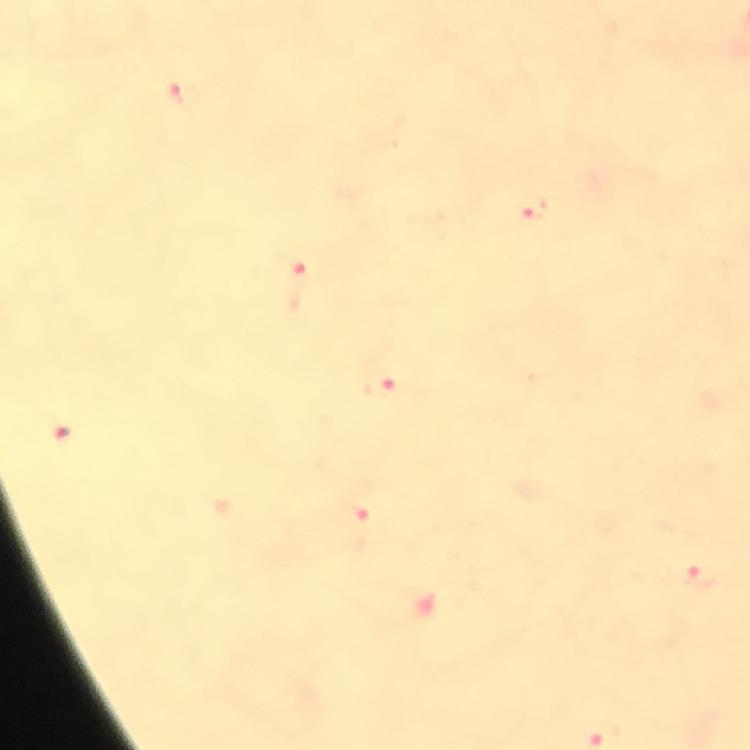

stain = Giemsa
context = from a malaria diagnostic workup
magnification = 100x
malaria parasite locations = approximate centers as [x, y] in pixels: [181, 94], [533, 208], [298, 282], [381, 385], [352, 525], [701, 576]
image size = 750×750 pixels
cropped from = one field of view
preparation = thick smear
immersion oil = applied
capture = smartphone mounted on the microscope